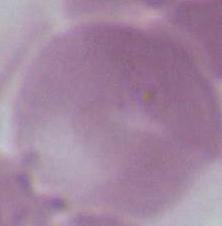
Micrograph. A red blood cell is shown. Captured at 1000x magnification.